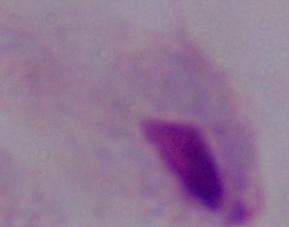
Micrograph. Captured at 1000x magnification. A trichomonad is shown.